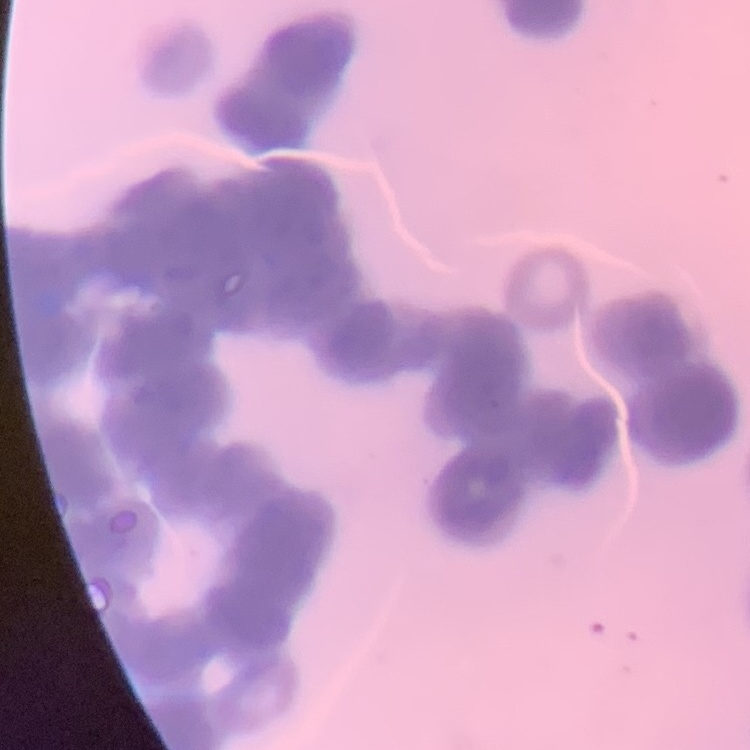

red blood cell morphology = rouleaux formation
stain = Field's or Giemsa
image type = one tile cut from a larger photomicrograph
preparation = thin blood smear